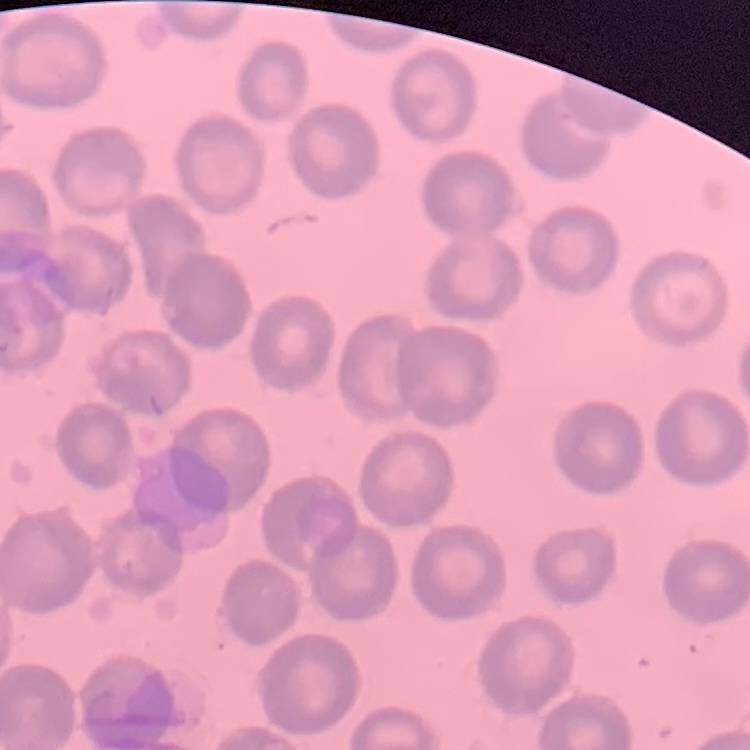
Summary:
  - Erythrocyte morphology: no rouleaux formation
  - Stain: Field's or Giemsa
  - Preparation: thin peripheral smear
  - Image type: square crop of a larger photomicrograph